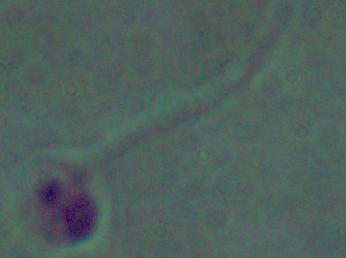
Photomicrograph. 1000x magnification. A Leishmania parasite is shown.